Comment on the morphology of the erythrocytes.
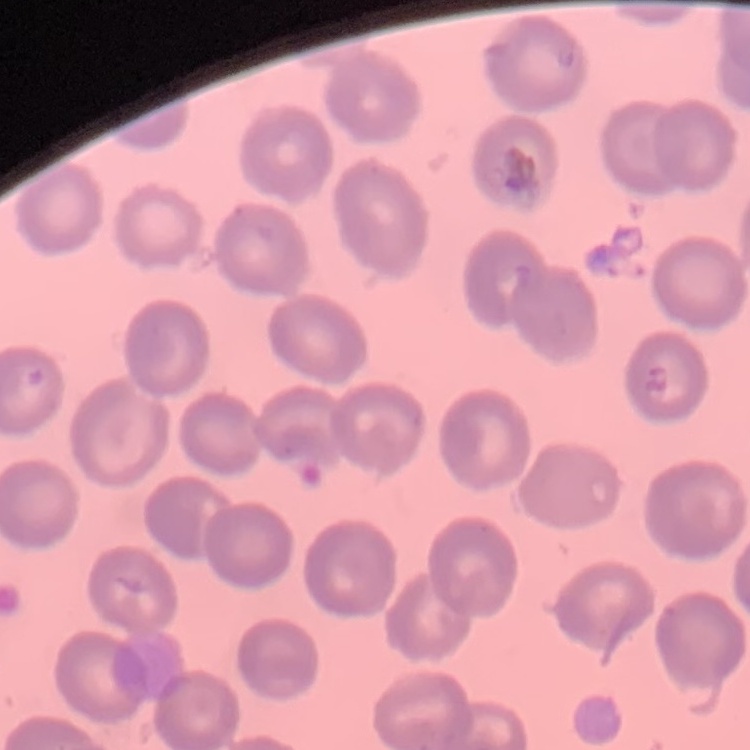

No rouleaux formation.

Square crop of a larger photomicrograph. Thin blood film. Field's or Giemsa stain.